Name the parasite shown.
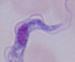
This is a trypanosome.

magnification = 1000x
modality = photomicrograph